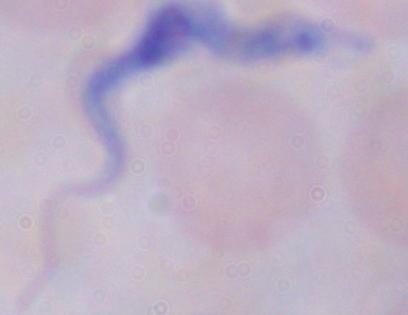

{
  "magnification": "1000x",
  "identification": "trypanosome",
  "modality": "photomicrograph"
}